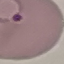 Malaria status: parasitized. Cell patch, automatically extracted from a larger field of view and resized to 64 × 64 pixels. Giemsa stain. Thin blood smear. Photographed with a smartphone camera at the microscope eyepiece.